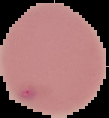

Summary:
  - Result: malaria parasites identified
  - Preparation: thin blood film
  - Image type: cell region segmented out of the field of view; surrounding area masked to black
  - Image size: 109×118 pixels